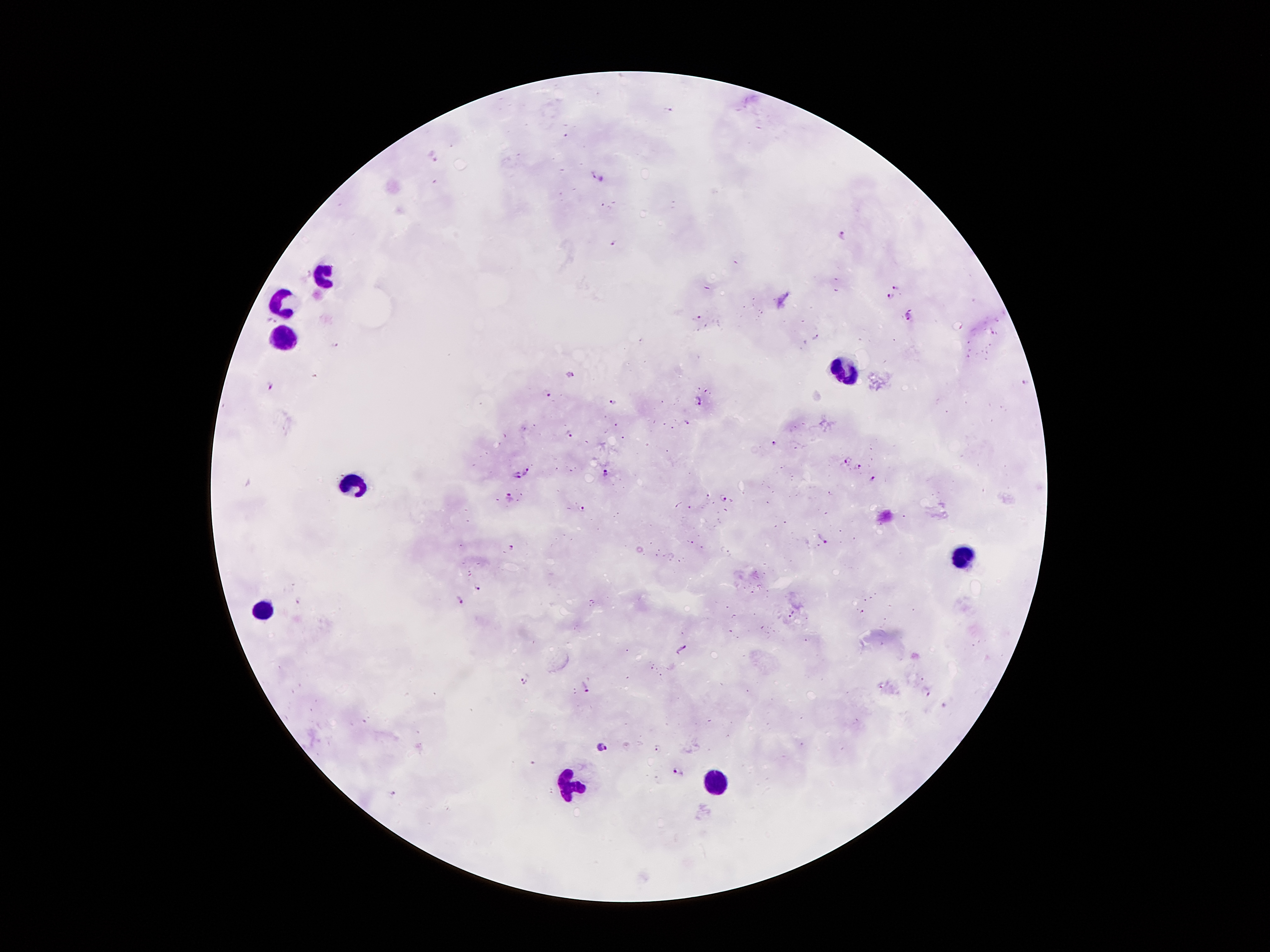
coordinate format = approximate object centers, in pixels from the top-left corner
Plasmodium parasite locations = (x=670, y=108), (x=595, y=175), (x=842, y=234), (x=616, y=242), (x=897, y=287), (x=890, y=297), (x=908, y=317), (x=698, y=318), (x=998, y=319), (x=272, y=320), (x=992, y=333), (x=337, y=344), (x=569, y=374), (x=1026, y=382), (x=271, y=387), (x=550, y=396), (x=699, y=401), (x=614, y=403), (x=688, y=422), (x=569, y=434), (x=774, y=442), (x=845, y=460), (x=859, y=468), (x=528, y=471), (x=604, y=473), (x=517, y=476), (x=873, y=480), (x=723, y=497), (x=509, y=498), (x=584, y=508), (x=824, y=539), (x=513, y=547), (x=476, y=585), (x=460, y=600), (x=299, y=601), (x=862, y=611), (x=792, y=614), (x=681, y=648), (x=523, y=681), (x=585, y=687), (x=926, y=692), (x=603, y=747), (x=659, y=749), (x=678, y=770), (x=395, y=794)
leukocyte locations = (x=324, y=277), (x=284, y=299), (x=284, y=340), (x=847, y=373), (x=354, y=485), (x=963, y=556), (x=261, y=610), (x=717, y=784), (x=570, y=786)
stain = Giemsa
field of view = one from this slide
patient malaria status = positive for Plasmodium falciparum
magnification = 100x
preparation = thick peripheral-blood smear
capture = smartphone camera through the microscope eyepiece
image size = 1270×952 pixels